Report the malaria status of this cell.
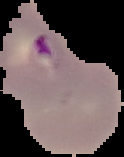

It is parasitized.

{
  "image_size": "124×157 pixels",
  "preparation": "thin blood film",
  "image_type": "segmented cell region with the area outside set to black"
}